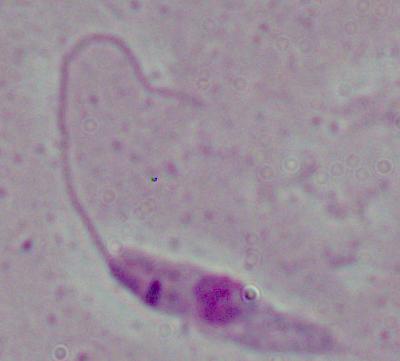
Summary:
  - Magnification: 1000x
  - Modality: micrograph
  - Identification: Leishmania